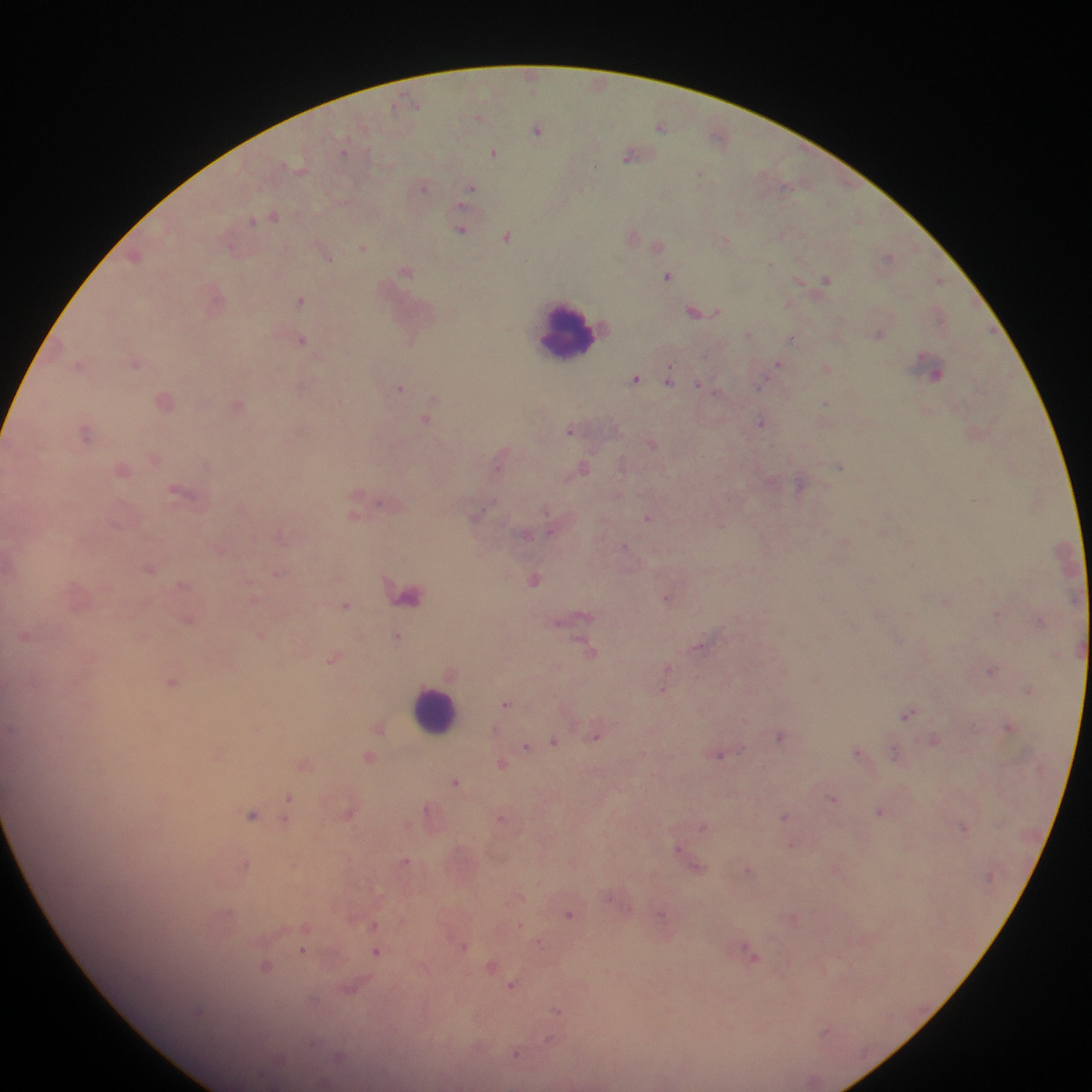

image size = 1092×1092 pixels
country = Ghana
capture = mobile-phone photograph through a microscope
leukocyte locations = approximate centers as [x, y] in pixels: [565, 328], [438, 713]
malaria parasite locations = approximate centers as [x, y] in pixels: [530, 73], [393, 107], [660, 127], [537, 130], [494, 152], [634, 154], [629, 157], [596, 168], [423, 187], [472, 188], [581, 189], [462, 206], [461, 230], [724, 240], [363, 247], [331, 259], [772, 263], [406, 271], [667, 276], [826, 280], [801, 281], [301, 300], [720, 310], [694, 312], [748, 333], [880, 335], [793, 338], [303, 341], [779, 363], [672, 364], [827, 367], [938, 374], [636, 379], [764, 379], [669, 382], [699, 385], [401, 388], [826, 404], [426, 419], [761, 422], [569, 432], [840, 466], [585, 468], [121, 470], [547, 510], [624, 545], [149, 569], [997, 614], [398, 635], [697, 647], [667, 667], [991, 672], [172, 681], [725, 683], [665, 688], [506, 704], [909, 714], [745, 721], [1008, 725], [597, 737], [781, 738], [553, 741], [526, 746], [856, 752], [721, 754], [218, 756], [304, 764], [500, 764], [456, 782], [834, 797], [289, 798], [426, 808], [880, 812], [252, 814], [785, 816], [500, 818], [284, 819], [704, 827], [965, 827], [648, 832], [791, 845], [677, 847], [840, 860], [405, 862], [247, 864], [294, 864], [749, 869], [661, 913], [569, 914], [522, 924], [375, 925], [308, 927], [539, 943], [464, 946], [304, 950], [376, 951], [267, 964], [492, 966], [513, 985], [556, 1010], [826, 1029], [552, 1039], [516, 1054]
preparation = thick blood film
field of view = single